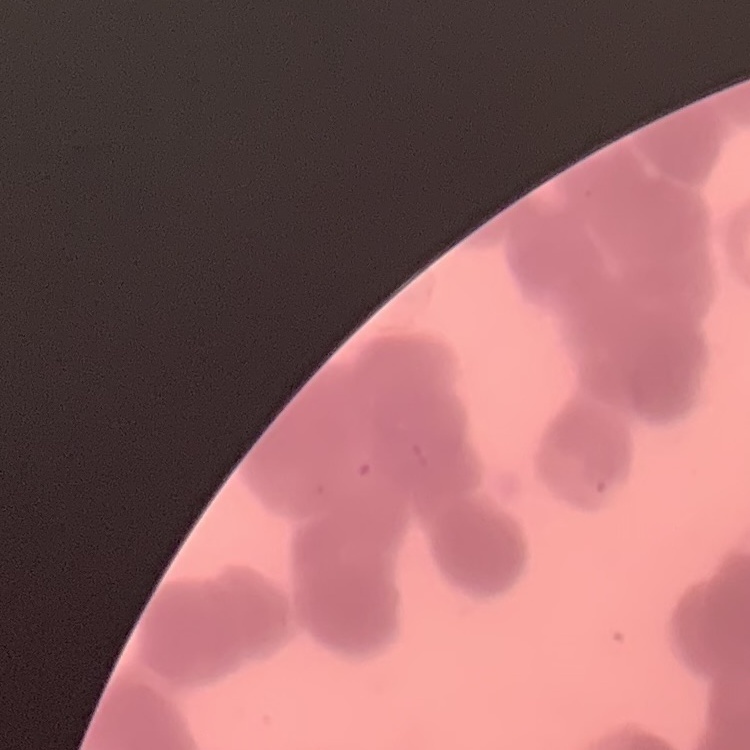
red blood cell morphology = rouleaux formation
image type = one tile cut from a larger photomicrograph
stain = Field's or Giemsa
preparation = thin peripheral smear